Assess the morphology of the red blood cells.
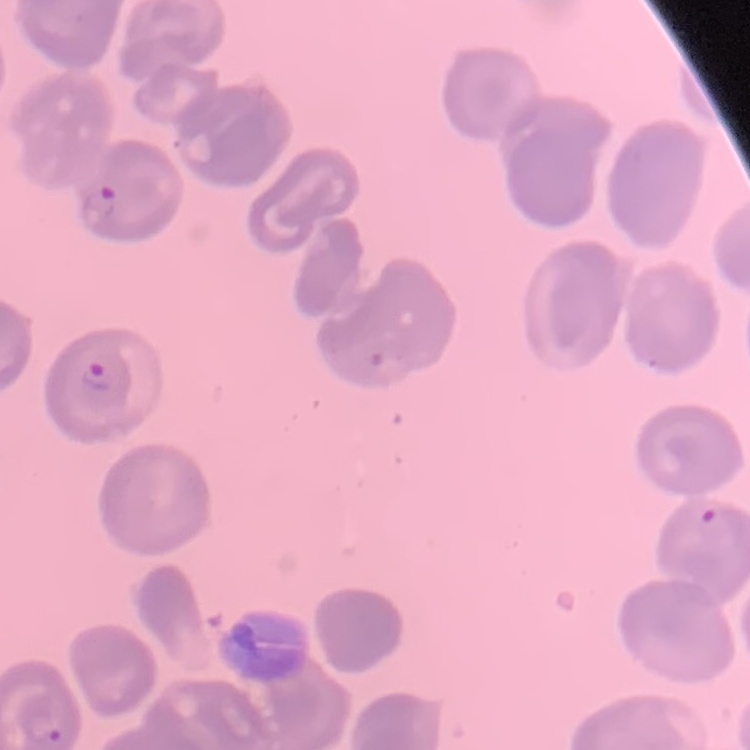
No rouleaux formation.

image type = square crop of a larger photomicrograph
stain = Field's or Giemsa
preparation = thin blood smear